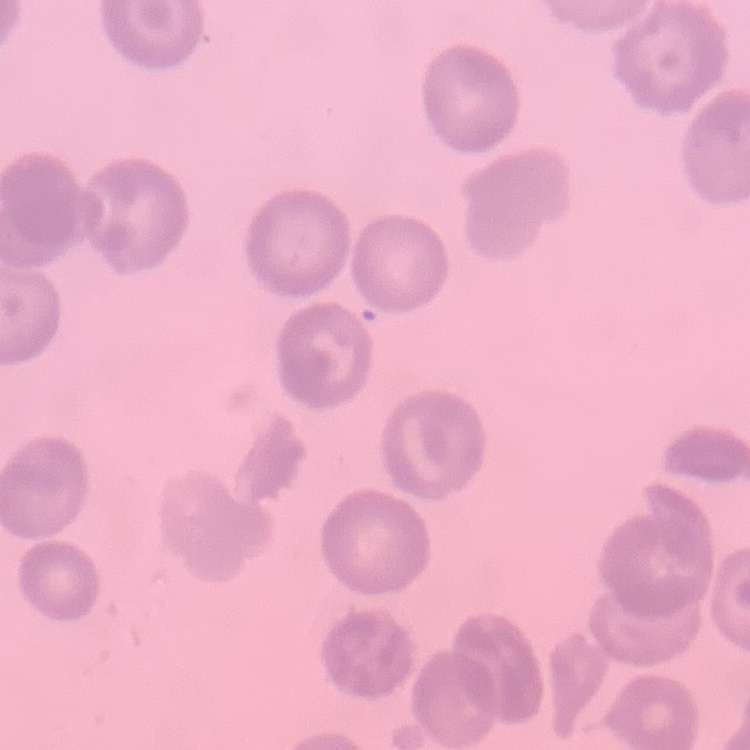
Summary:
  - Red blood cell morphology: no rouleaux formation
  - Stain: Field's or Giemsa
  - Preparation: thin blood smear
  - Image type: square crop of a larger photomicrograph